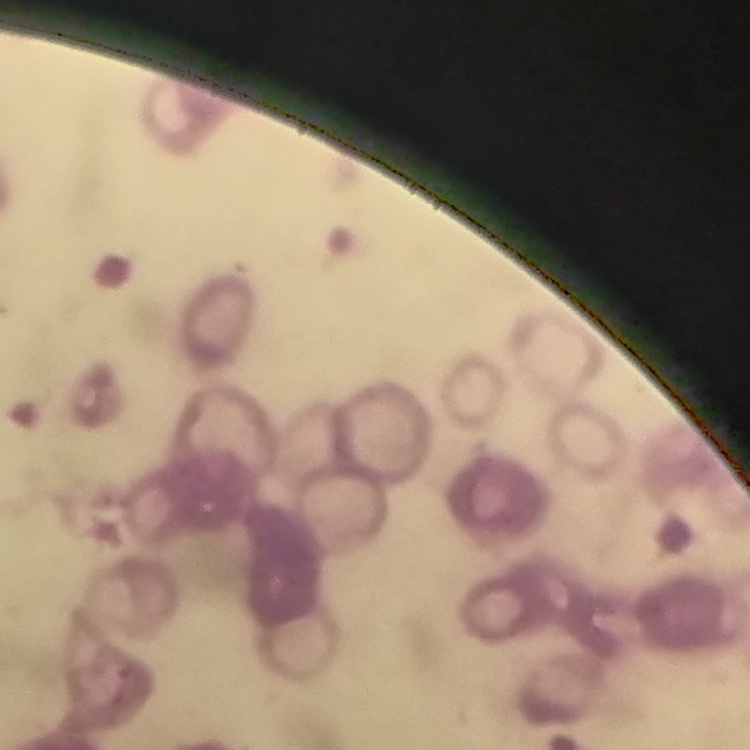
red blood cell morphology = rouleaux formation
stain = Field's or Giemsa
image type = square crop of a larger photomicrograph
preparation = thin peripheral smear